Report the malaria status of this cell.
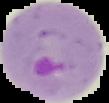

It is parasitized.

image type = segmented cell region with the area outside set to black
image size = 109×103 pixels
preparation = thin blood smear